Outline each blood parasite and name the species.
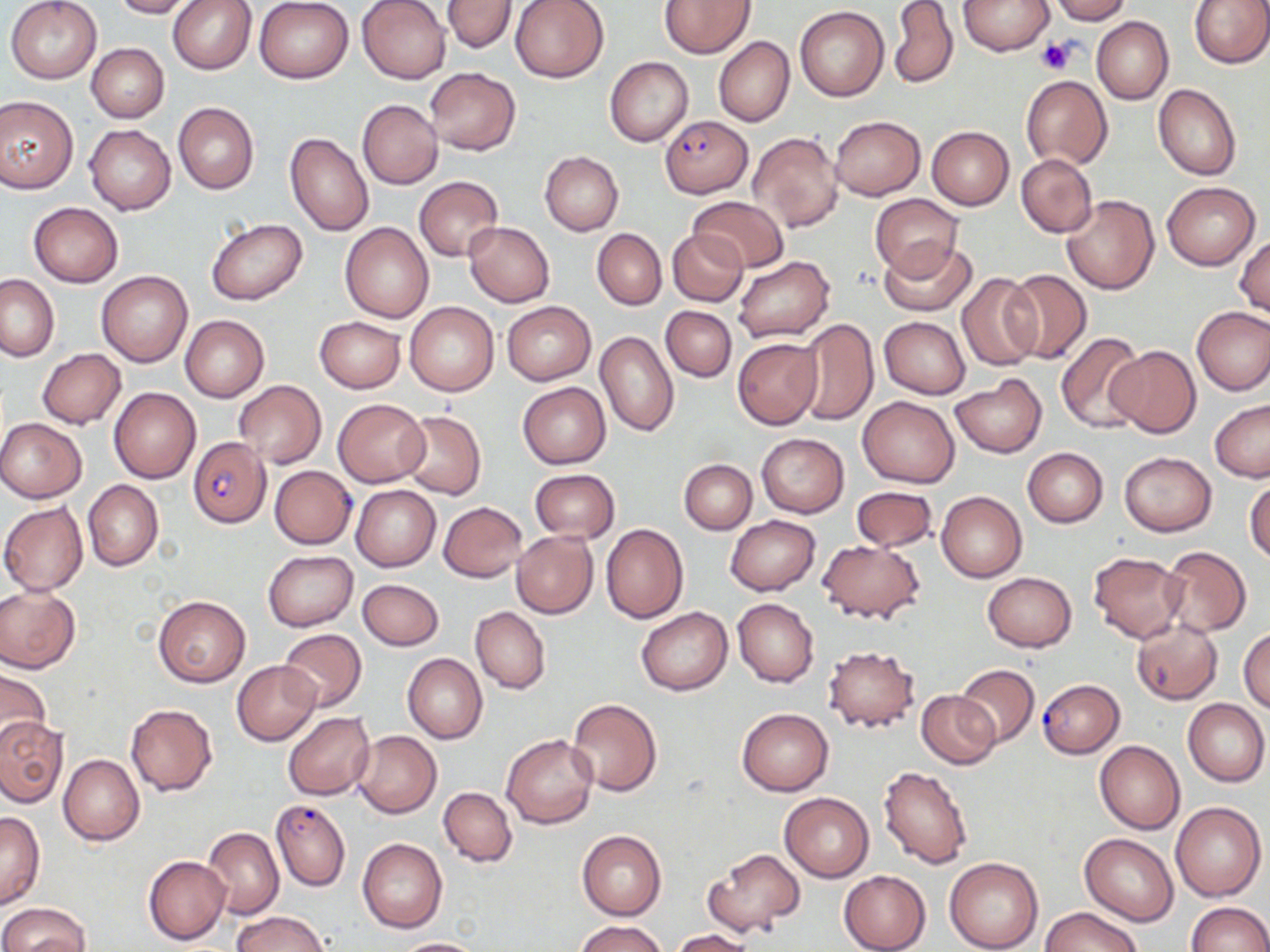

Approximate bounding boxes as [x1, y1, x2, y2] in pixels.
Plasmodium falciparum-infected red blood cells: [660, 116, 752, 198], [187, 438, 271, 527], [1037, 679, 1125, 758], [270, 799, 350, 891].
No Plasmodium ovale, Plasmodium malariae, Plasmodium vivax, Babesia divergens, or Trypanosoma brucei observed.

Summary:
  - Uninfected red blood cell locations: [5, 0, 103, 84], [109, 0, 197, 18], [167, 0, 256, 74], [254, 0, 355, 83], [357, 0, 451, 84], [440, 0, 520, 53], [509, 0, 611, 83], [660, 0, 754, 57], [958, 0, 1053, 55], [1049, 0, 1131, 23], [1188, 0, 1270, 68], [889, 1, 958, 90], [795, 6, 889, 101], [1091, 16, 1173, 104], [714, 37, 794, 127], [87, 43, 168, 122], [605, 55, 694, 147], [425, 68, 520, 154], [1021, 75, 1113, 169], [1153, 83, 1241, 181], [0, 96, 78, 194], [357, 99, 443, 189], [172, 102, 258, 194], [830, 116, 925, 200], [86, 124, 176, 214], [926, 126, 1015, 209], [285, 132, 373, 236], [749, 132, 844, 234], [540, 152, 623, 234], [1016, 154, 1097, 237], [415, 177, 503, 261], [1162, 181, 1259, 271], [869, 194, 964, 281], [1062, 195, 1159, 294], [689, 197, 789, 272], [28, 203, 123, 287], [205, 218, 308, 305], [339, 223, 433, 323], [464, 223, 555, 306], [592, 228, 667, 310], [668, 229, 748, 306], [1234, 234, 1269, 318], [878, 238, 979, 317], [732, 255, 836, 343], [97, 271, 192, 366], [1003, 271, 1092, 364], [957, 272, 1042, 371], [0, 274, 58, 361], [501, 301, 596, 385], [404, 302, 499, 397], [661, 306, 736, 381], [1192, 306, 1270, 395], [181, 315, 269, 402], [314, 316, 405, 392], [880, 316, 970, 398], [794, 319, 879, 426], [595, 331, 679, 438], [1056, 332, 1146, 433], [733, 337, 822, 429], [1106, 345, 1200, 437], [37, 348, 126, 428], [950, 375, 1047, 457], [234, 380, 326, 468], [518, 382, 611, 468], [108, 387, 201, 483], [858, 396, 959, 487], [333, 399, 429, 485], [1210, 399, 1270, 482], [400, 411, 486, 500], [0, 418, 86, 503], [756, 432, 849, 517], [1022, 447, 1108, 527], [1120, 452, 1217, 536], [679, 460, 757, 534], [270, 466, 356, 548], [529, 469, 620, 543], [1246, 475, 1270, 564], [83, 480, 163, 570], [351, 485, 441, 571], [852, 486, 937, 551], [936, 491, 1027, 582], [438, 501, 527, 581], [0, 502, 88, 596], [725, 516, 820, 596], [600, 524, 688, 625], [511, 530, 598, 618], [817, 540, 926, 624], [1160, 546, 1251, 637], [262, 550, 358, 631], [1088, 551, 1187, 643], [982, 572, 1076, 652], [357, 578, 444, 650], [0, 586, 80, 673], [153, 594, 250, 687], [733, 598, 818, 687], [471, 607, 550, 694], [637, 607, 732, 695], [1130, 620, 1223, 704], [1239, 627, 1270, 714], [278, 628, 367, 711], [822, 644, 921, 734], [403, 653, 488, 744], [232, 661, 321, 744], [955, 664, 1039, 747], [0, 669, 52, 752], [916, 689, 999, 769], [566, 698, 663, 797], [1183, 698, 1269, 786], [125, 703, 217, 796], [736, 707, 834, 796], [282, 711, 374, 801], [0, 718, 67, 805], [354, 730, 442, 818], [502, 735, 597, 828], [1094, 741, 1185, 834], [58, 753, 144, 845], [879, 765, 976, 869], [438, 786, 517, 867], [780, 792, 873, 881], [1170, 802, 1265, 901], [0, 812, 45, 909], [203, 827, 284, 920], [577, 830, 666, 920], [1079, 834, 1179, 925], [357, 838, 447, 933], [704, 847, 805, 936], [144, 855, 230, 945], [944, 857, 1043, 952], [837, 870, 932, 952], [0, 902, 89, 952], [1185, 902, 1270, 951], [1041, 906, 1140, 952], [232, 912, 331, 952], [576, 920, 666, 952], [670, 929, 755, 951], [389, 937, 487, 951]
  - Platelet locations: [1036, 38, 1076, 75]
  - Slide-level diagnosis: Plasmodium falciparum
  - Magnification: 1000x
  - Field of view: one of a larger specimen
  - Stain: May-Grünwald-Giemsa
  - Preparation: thin blood smear
  - Modality: light microscopy
  - Image size: 1270×952 pixels